Locate platelets.
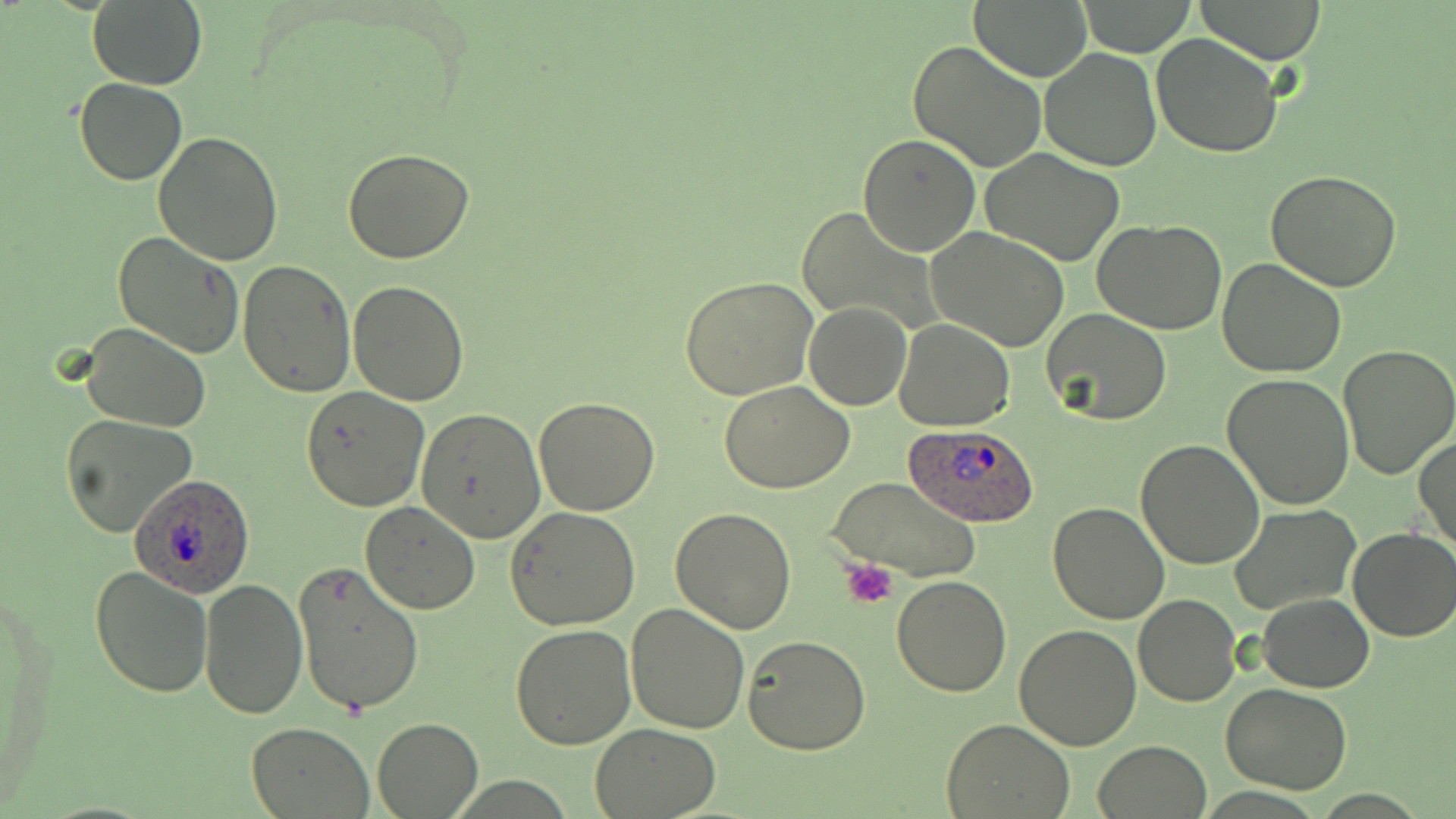

Approximate bounding boxes as (x1,y1)-(x2,y2) corner pairs in pixels.
Platelets: (842,560)-(898,611).

Summary:
  - Plasmodium ovale-infected red blood cell locations: (901,420)-(1037,529), (128,472)-(256,596)
  - Uninfected red blood cell locations: (88,0)-(207,91), (969,0)-(1091,83), (1193,0)-(1328,64), (1075,1)-(1199,56), (1151,33)-(1283,157), (907,38)-(1048,174), (1040,48)-(1161,170), (74,77)-(189,185), (152,131)-(285,265), (859,134)-(982,257), (342,146)-(475,263), (979,149)-(1126,266), (1265,171)-(1401,293), (795,206)-(931,334), (1092,217)-(1228,336), (928,227)-(1070,351), (112,230)-(244,359), (1217,257)-(1347,376), (238,260)-(356,396), (679,276)-(819,399), (349,281)-(469,405), (804,302)-(911,411), (1043,309)-(1170,425), (894,320)-(1016,431), (77,323)-(212,433), (1338,345)-(1456,478), (1222,373)-(1355,510), (720,381)-(856,493), (300,386)-(429,511), (534,396)-(659,515), (416,408)-(545,542), (61,414)-(196,538), (1415,434)-(1455,557), (1135,439)-(1265,570), (826,476)-(981,582), (360,501)-(481,613), (1047,502)-(1168,624), (1231,504)-(1360,615), (504,506)-(641,630), (671,506)-(796,633), (1347,528)-(1456,642), (291,560)-(424,716), (90,565)-(214,699), (891,573)-(1013,696), (198,576)-(309,719), (1258,593)-(1373,692), (1133,594)-(1241,707), (624,602)-(751,736), (1014,624)-(1143,749), (511,626)-(637,749), (741,633)-(872,754), (1222,684)-(1353,795), (372,717)-(484,817), (942,717)-(1076,818), (247,722)-(373,817), (590,722)-(721,817), (1095,740)-(1212,818)
  - Slide-level diagnosis: Plasmodium ovale
  - Magnification: 1000x
  - Stain: May-Grünwald-Giemsa
  - Image size: 1456×819 pixels
  - Modality: light microscopy
  - Preparation: thin blood film
  - Field of view: one of a larger specimen